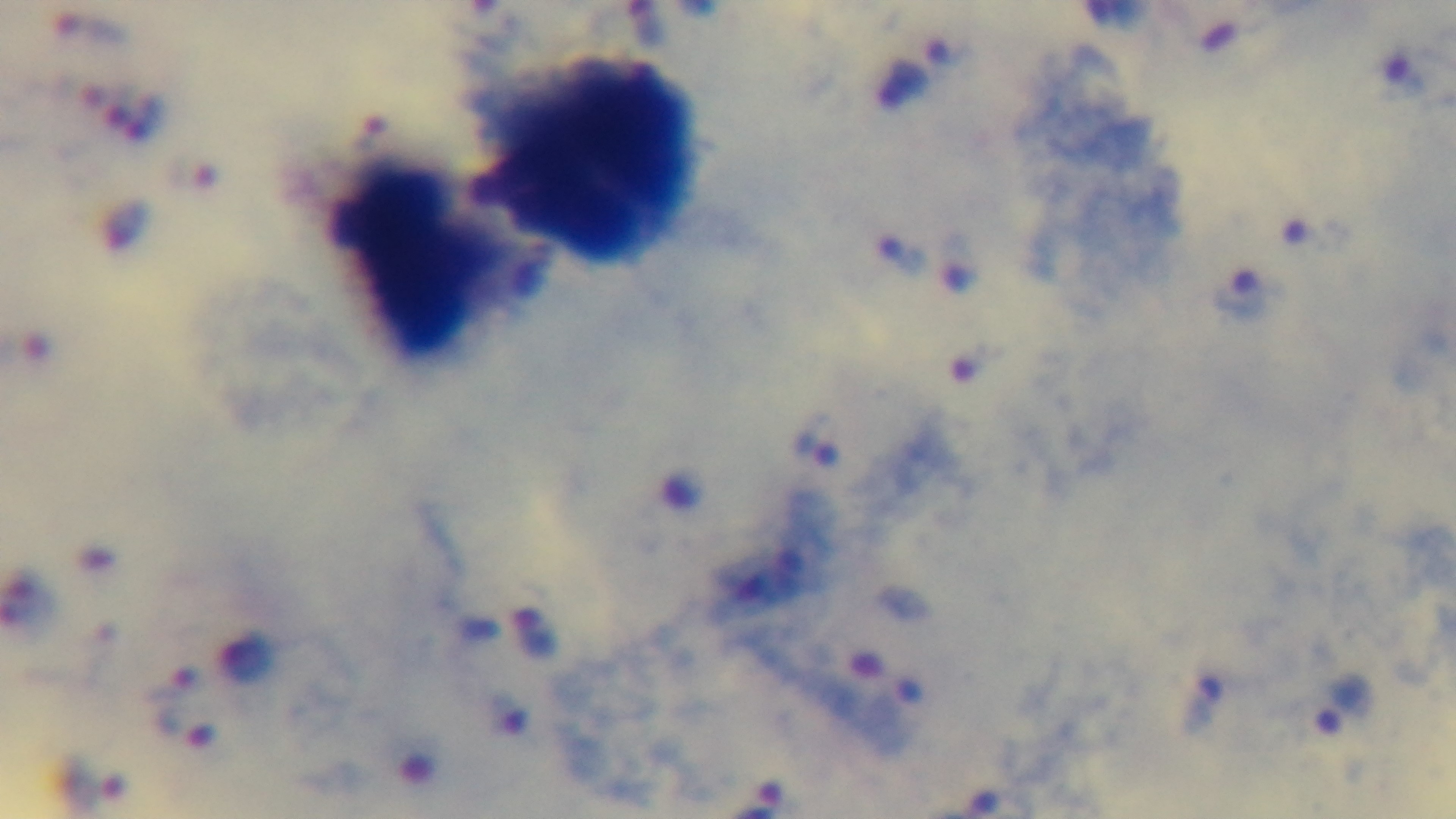

100x oil-immersion objective. Light microscopy. Single field of view. Giemsa stain. Malaria status: infected. Mounted 4K digital camera. Preparation: thick blood film.